Classify this cell by malaria status.
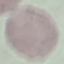
It is uninfected.

stain = Giemsa
image type = automatically extracted cell patch, resized to 64 × 64 pixels
preparation = thin blood film
capture = smartphone through the microscope eyepiece